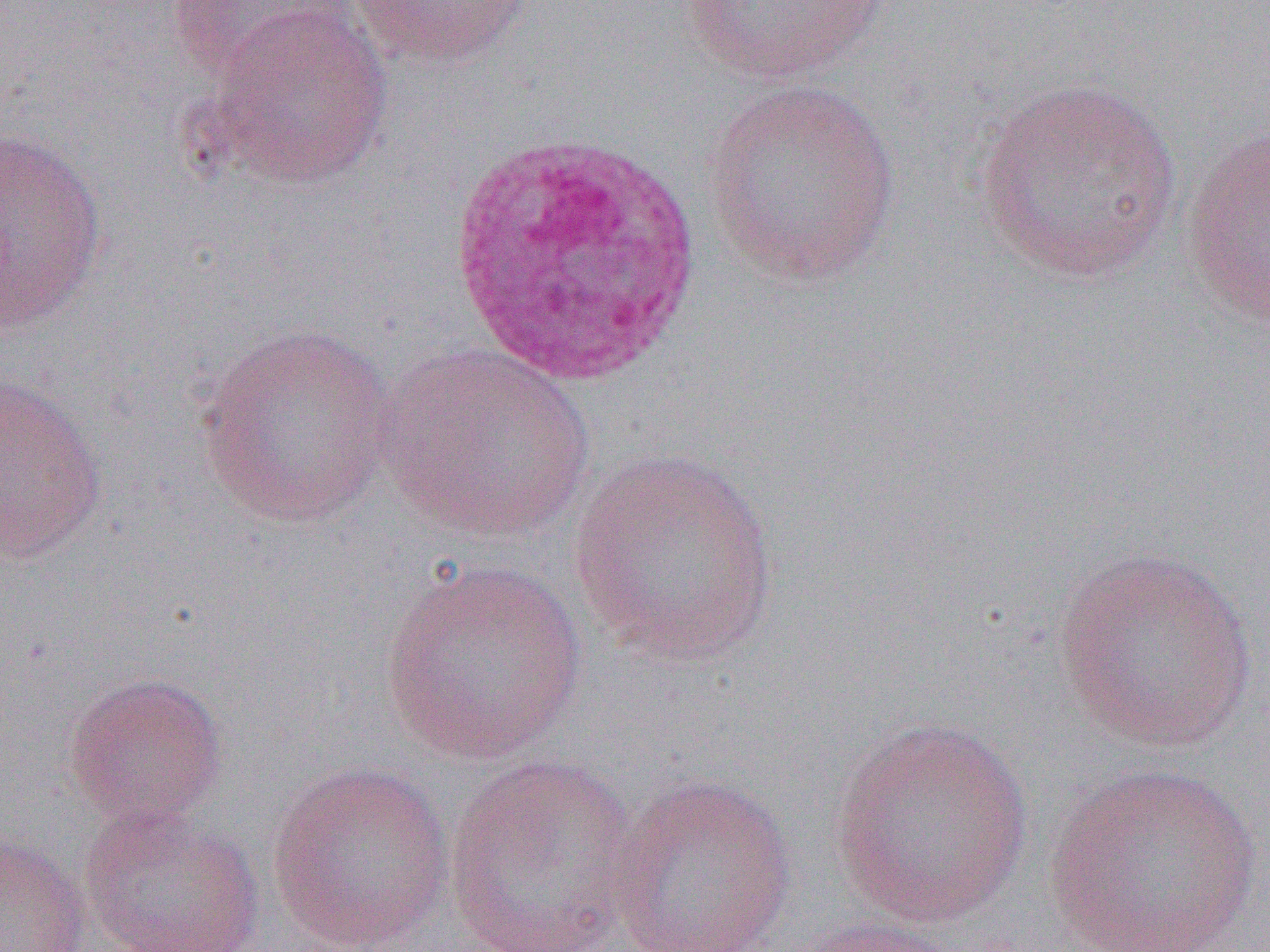
Approximate bounding boxes as (x1, y1, x2, y2) in pixels. White blood cell locations: (445, 130, 710, 392). Uninfected red blood cell locations: (349, 0, 536, 70), (677, 0, 897, 85), (166, 1, 362, 81), (196, 5, 394, 192), (972, 78, 1184, 285), (703, 81, 903, 288), (1180, 124, 1270, 330), (0, 126, 109, 335), (195, 322, 399, 531), (372, 344, 598, 543), (0, 370, 110, 566), (567, 446, 784, 667), (1051, 546, 1260, 753), (380, 560, 588, 765), (63, 670, 228, 828), (829, 717, 1034, 927), (444, 754, 643, 951), (266, 761, 456, 951), (1043, 762, 1265, 950), (608, 772, 797, 952), (79, 807, 267, 952), (0, 832, 91, 952), (783, 917, 967, 952). Slide-level diagnosis: Plasmodium ovale. Optical microscopy. Single field of view. Image is 1270×952 pixels. Captured at 1000x magnification. Thin blood smear.